Assess for malaria.
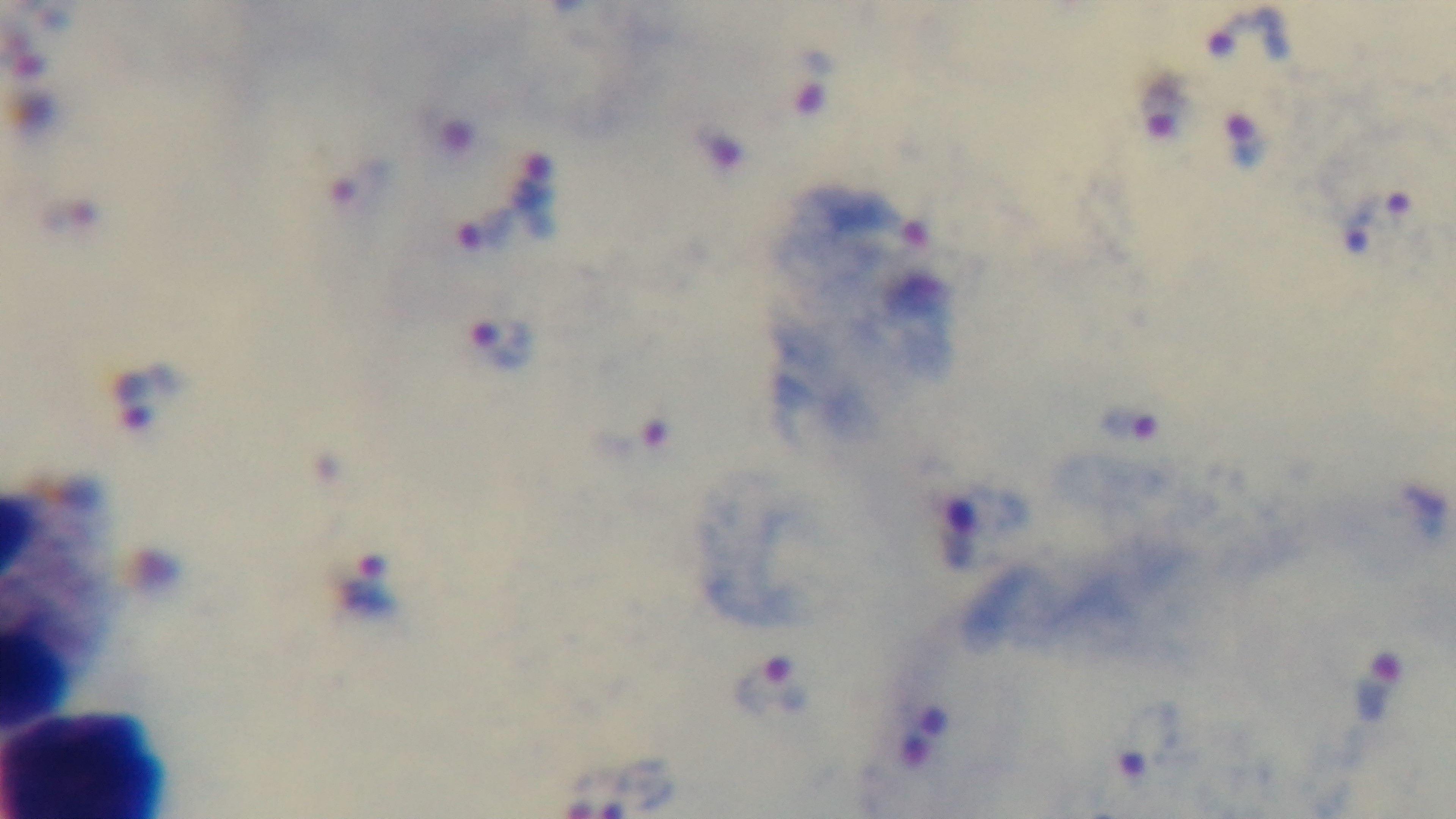
Positive.

Summary:
  - Capture: mounted 4K digital camera
  - Field of view: one from the slide
  - Objective: 100x oil immersion
  - Stain: Giemsa
  - Modality: light microscopy
  - Preparation: thick blood film